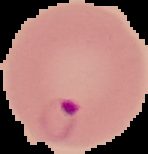
Summary:
  - Image size: 148×154 pixels
  - Image type: segmented cell region on a black background
  - Result: malaria parasites detected
  - Preparation: thin blood film